Locate every Plasmodium parasite and every leukocyte.
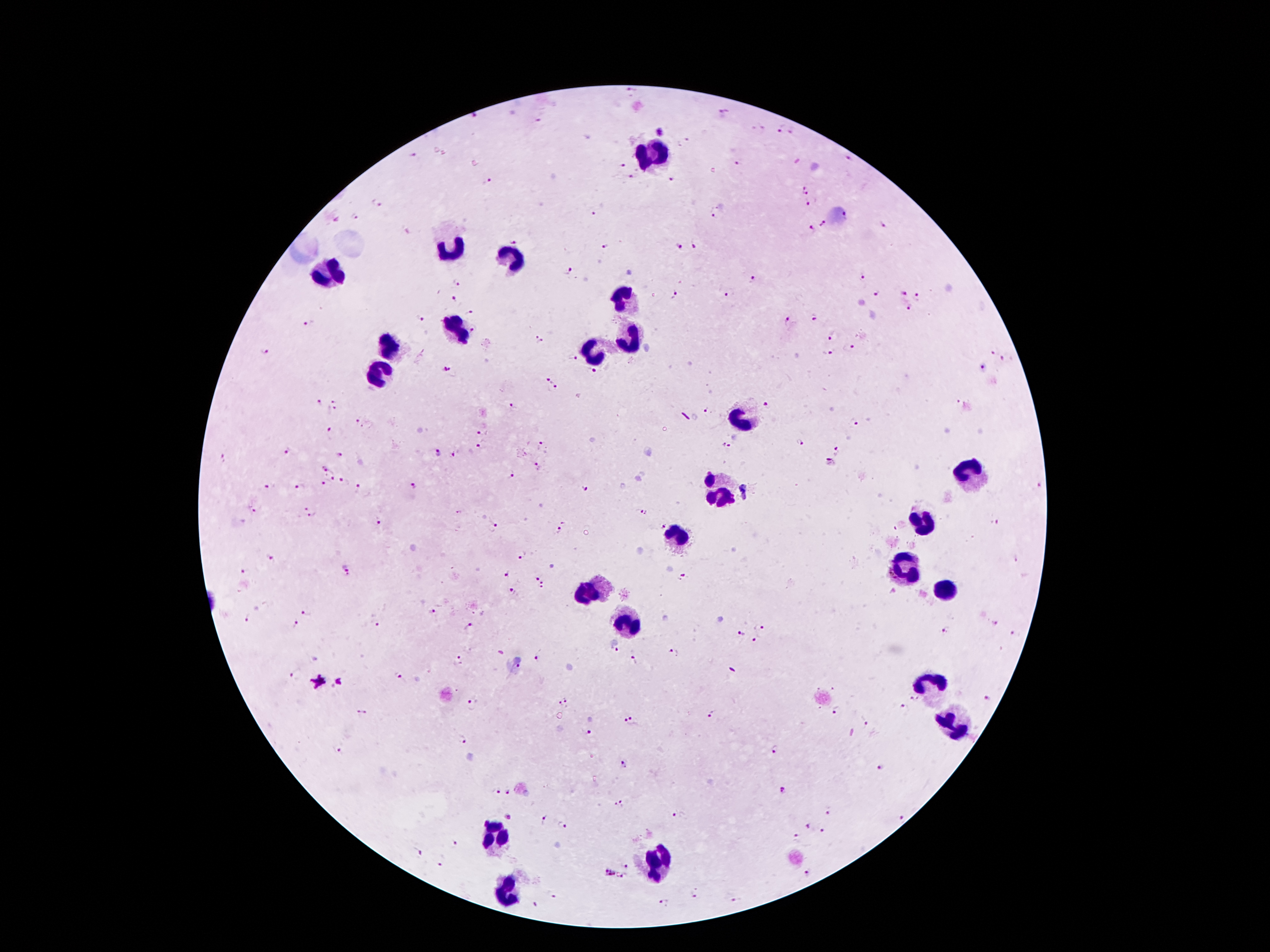
Approximate centers as {x, y} in pixels.
Plasmodium parasites: {629, 89}, {724, 114}, {475, 119}, {540, 123}, {780, 129}, {792, 130}, {660, 133}, {415, 155}, {846, 159}, {741, 163}, {620, 166}, {629, 178}, {672, 180}, {489, 182}, {807, 187}, {377, 203}, {809, 205}, {594, 212}, {716, 212}, {356, 216}, {824, 225}, {881, 226}, {809, 231}, {516, 238}, {696, 245}, {604, 246}, {679, 247}, {567, 270}, {861, 277}, {750, 279}, {458, 284}, {673, 293}, {728, 294}, {877, 294}, {904, 295}, {454, 299}, {919, 300}, {908, 309}, {470, 313}, {420, 316}, {813, 318}, {786, 321}, {310, 323}, {473, 329}, {832, 336}, {537, 341}, {850, 348}, {993, 350}, {266, 351}, {828, 354}, {573, 358}, {1004, 360}, {446, 368}, {981, 368}, {593, 371}, {547, 381}, {556, 388}, {319, 401}, {958, 403}, {335, 405}, {768, 405}, {513, 407}, {706, 411}, {357, 418}, {855, 423}, {366, 427}, {331, 430}, {482, 431}, {799, 443}, {543, 445}, {726, 446}, {481, 447}, {288, 451}, {837, 451}, {438, 452}, {339, 455}, {453, 455}, {224, 458}, {830, 464}, {538, 466}, {325, 468}, {511, 474}, {332, 478}, {346, 482}, {324, 485}, {414, 485}, {269, 486}, {360, 486}, {300, 487}, {1040, 487}, {583, 488}, {747, 491}, {255, 511}, {643, 511}, {311, 512}, {378, 523}, {998, 523}, {662, 525}, {495, 528}, {559, 531}, {522, 556}, {271, 557}, {1016, 560}, {348, 568}, {246, 570}, {508, 573}, {534, 576}, {682, 579}, {543, 585}, {513, 591}, {306, 611}, {431, 612}, {248, 620}, {995, 623}, {761, 624}, {297, 625}, {378, 625}, {470, 625}, {946, 632}, {740, 634}, {1012, 634}, {756, 640}, {615, 652}, {673, 652}, {538, 657}, {636, 658}, {460, 660}, {518, 667}, {294, 673}, {399, 675}, {319, 683}, {913, 698}, {989, 698}, {564, 701}, {470, 706}, {903, 706}, {835, 712}, {361, 714}, {711, 715}, {631, 721}, {863, 722}, {589, 732}, {463, 740}, {338, 749}, {774, 750}, {623, 765}, {880, 766}, {783, 791}, {496, 792}, {509, 792}, {619, 803}, {829, 813}, {677, 815}, {510, 817}, {902, 818}, {544, 819}, {564, 825}, {807, 827}, {823, 830}, {796, 838}, {453, 845}, {420, 853}, {440, 865}, {625, 865}, {609, 873}, {808, 874}, {625, 876}, {693, 892}, {553, 895}, {737, 900}, {665, 901}, {535, 904}.
Leukocytes: {653, 156}, {451, 246}, {512, 261}, {332, 271}, {626, 297}, {456, 328}, {632, 341}, {388, 347}, {594, 349}, {378, 374}, {741, 418}, {966, 472}, {718, 494}, {924, 525}, {680, 536}, {903, 563}, {945, 590}, {590, 593}, {628, 621}, {928, 689}, {953, 721}, {496, 836}, {655, 863}, {504, 891}.

Summary:
  - Magnification: 100x
  - Image size: 1270×952 pixels
  - Patient malaria status: positive for Plasmodium falciparum
  - Capture: smartphone through the microscope eyepiece
  - Preparation: thick peripheral-blood smear
  - Stain: Giemsa
  - Field of view: one from this slide